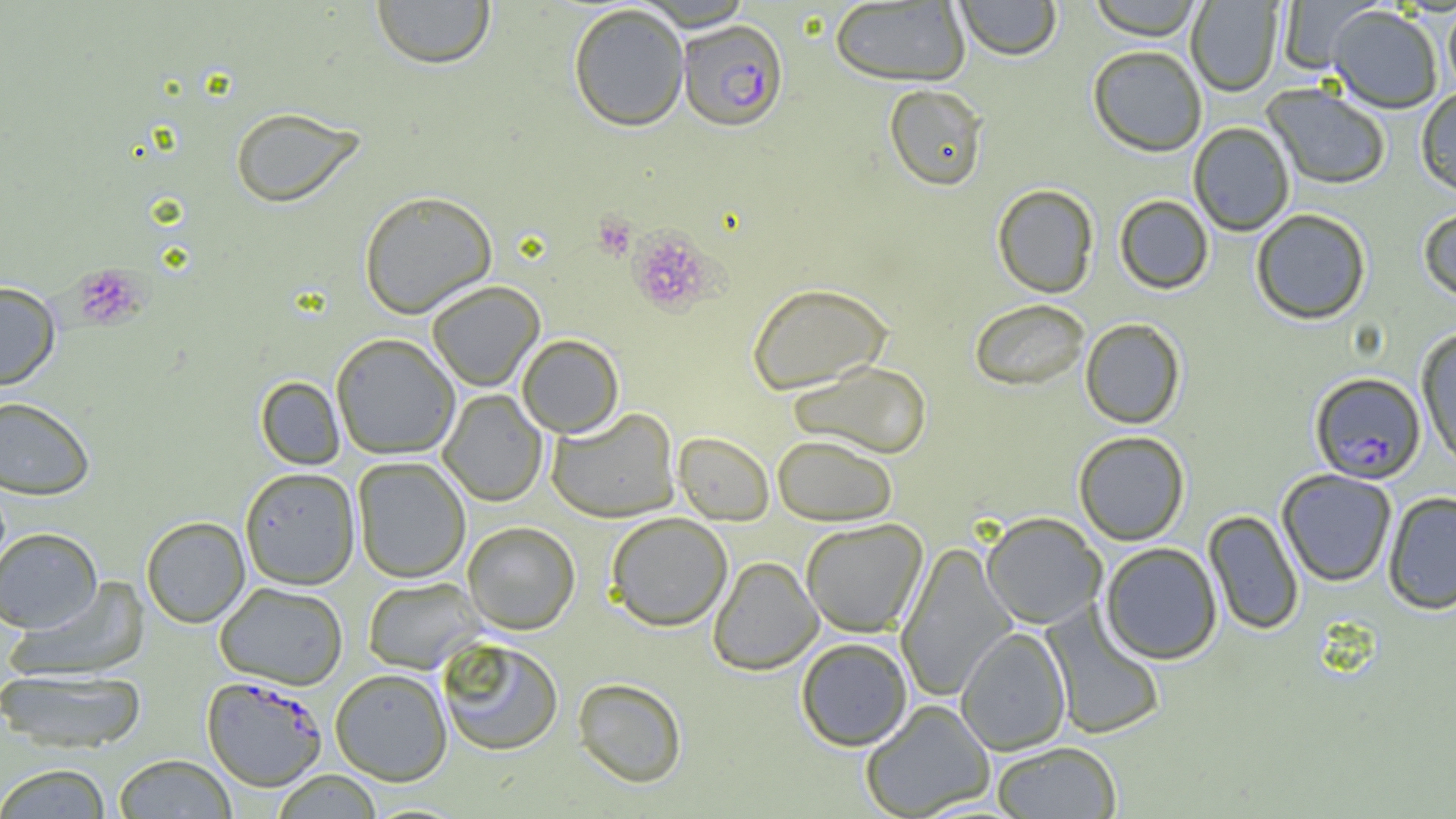

Summary:
  - Coordinate format: approximate bounding boxes as (x1,y1)-(x2,y2) corner pairs in pixels
  - Plasmodium falciparum-infected red blood cell locations: (676,19)-(788,131), (1309,371)-(1426,484), (202,674)-(327,790)
  - Uninfected red blood cell locations: (371,0)-(495,69), (954,0)-(1063,60), (1086,0)-(1205,40), (1277,0)-(1383,73), (829,1)-(970,86), (1186,1)-(1282,96), (568,2)-(689,131), (1443,4)-(1456,100), (1328,5)-(1443,113), (1088,45)-(1207,157), (884,84)-(988,191), (1262,84)-(1391,190), (1416,87)-(1456,197), (229,106)-(364,208), (1188,121)-(1295,236), (991,183)-(1099,298), (358,190)-(497,319), (1114,195)-(1214,294), (1418,206)-(1456,304), (1250,208)-(1372,325), (426,280)-(545,391), (0,281)-(60,390), (747,282)-(893,395), (969,298)-(1090,391), (1080,318)-(1186,429), (1416,326)-(1456,469), (331,332)-(460,459), (517,334)-(624,437), (788,360)-(932,459), (256,376)-(345,470), (438,389)-(548,507), (0,396)-(95,500), (546,407)-(680,523), (1073,430)-(1190,545), (673,432)-(774,525), (772,434)-(897,526), (352,456)-(470,583), (240,466)-(360,589), (1277,469)-(1397,587), (1382,491)-(1456,615), (1203,509)-(1304,635), (605,512)-(732,631), (980,512)-(1107,629), (141,515)-(250,628), (800,518)-(928,637), (462,521)-(580,635), (0,527)-(102,632), (896,542)-(1016,703), (1099,542)-(1223,664), (708,556)-(822,674), (7,577)-(152,682), (362,577)-(485,674), (214,581)-(348,689), (1041,603)-(1166,740), (955,626)-(1071,756), (437,637)-(564,756), (795,637)-(913,751), (0,667)-(149,753), (330,667)-(453,785), (572,677)-(687,788), (860,699)-(996,818), (991,741)-(1122,818), (113,754)-(238,818), (0,762)-(112,818), (270,770)-(383,818)
  - Platelet locations: (593,214)-(636,260), (626,228)-(717,315), (73,264)-(148,329)
  - Slide-level diagnosis: Plasmodium falciparum
  - Modality: optical microscopy
  - Magnification: 1000x
  - Image size: 1456×819 pixels
  - Field of view: single
  - Preparation: thin blood film